Locate every blood parasite and identify its species.
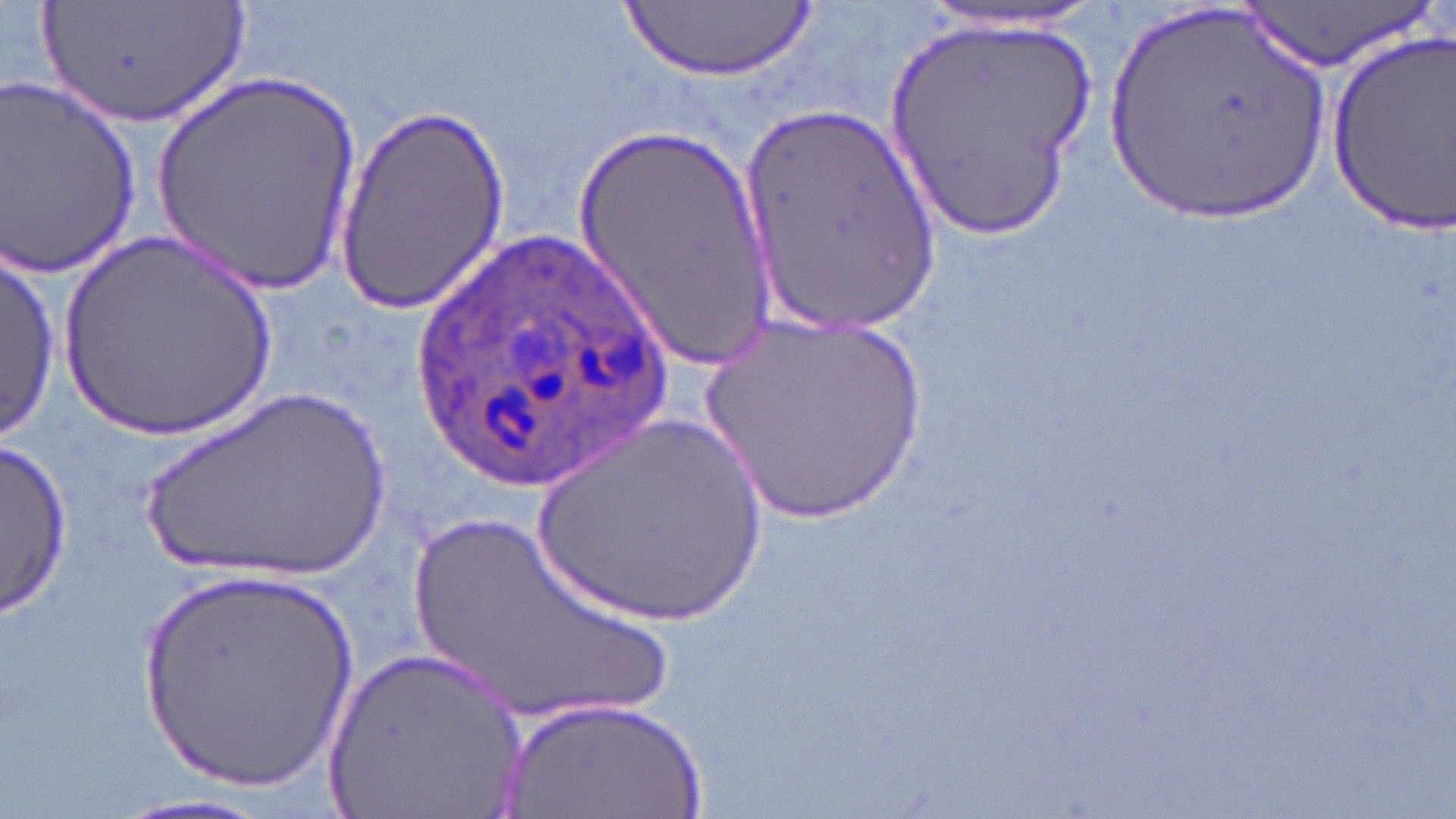
Approximate bounding boxes as [x1, y1, x2, y2] in pixels.
Plasmodium ovale-infected red blood cells: [399, 224, 680, 489].
No Plasmodium falciparum, Plasmodium malariae, Plasmodium vivax, Babesia divergens, or Trypanosoma brucei observed.

Summary:
  - Uninfected red blood cell locations: [39, 0, 253, 130], [920, 0, 1110, 33], [1103, 0, 1338, 227], [628, 1, 811, 82], [1238, 1, 1434, 75], [882, 17, 1102, 254], [1325, 28, 1456, 237], [150, 71, 365, 296], [1, 72, 144, 279], [737, 99, 948, 338], [337, 101, 509, 316], [573, 122, 776, 369], [58, 228, 284, 443], [0, 252, 59, 442], [693, 318, 936, 534], [132, 384, 400, 588], [532, 411, 771, 633], [2, 438, 75, 620], [406, 508, 679, 727], [130, 562, 368, 799], [323, 642, 529, 819], [498, 693, 714, 818], [93, 794, 308, 819]
  - Slide-level diagnosis: Plasmodium ovale
  - Modality: optical microscopy
  - Image size: 1456×819 pixels
  - Preparation: thin blood smear
  - Field of view: one of a larger specimen
  - Magnification: 1000x
  - Stain: May-Grünwald-Giemsa